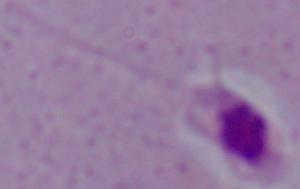
Summary:
  - Identification: Leishmania
  - Magnification: 1000x
  - Modality: micrograph